Locate every malaria parasite and identify its life-cycle stage.
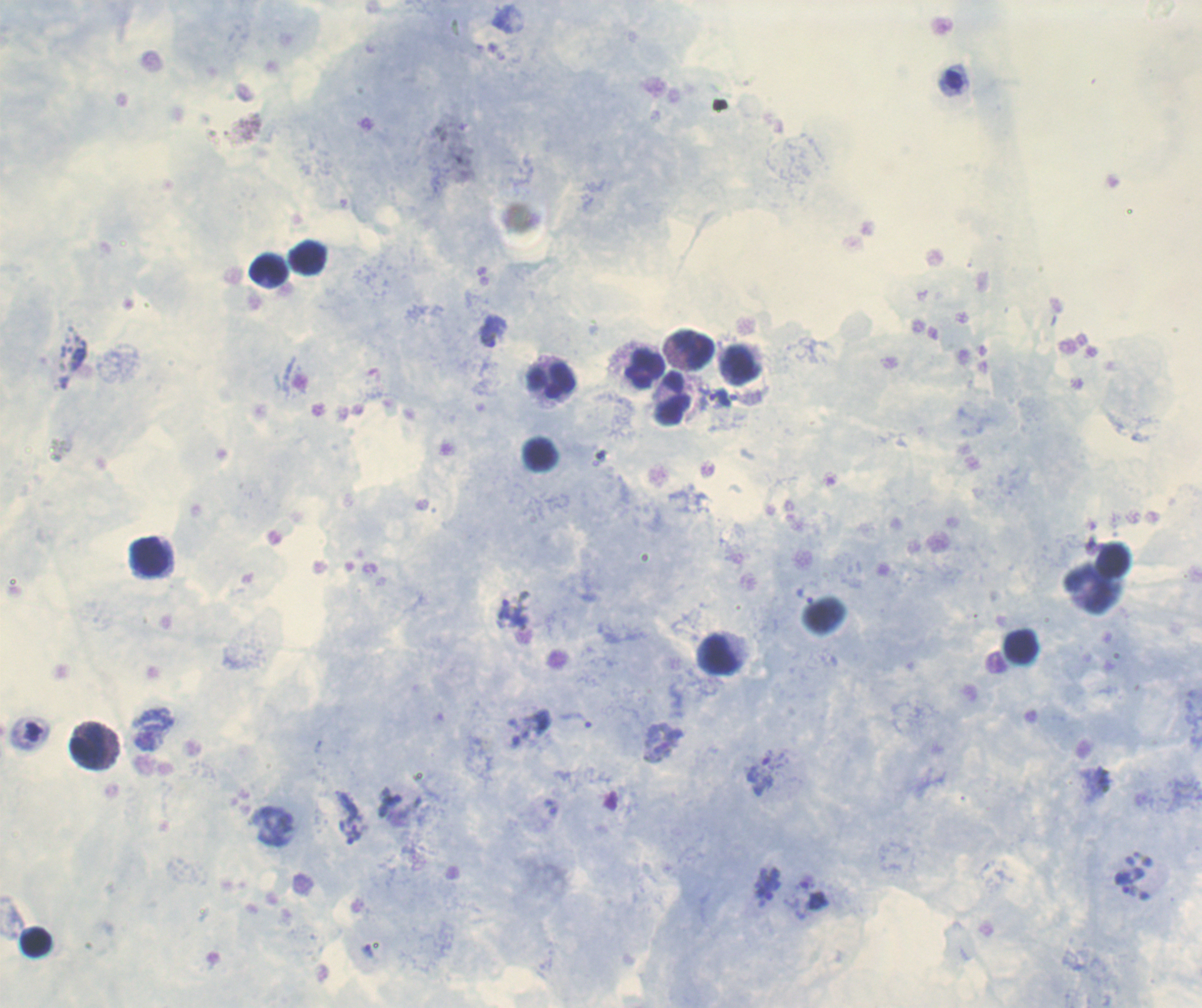

Approximate centers as [x, y] in pixels.
Trophozoites: [488, 340], [718, 397], [509, 612], [577, 720], [661, 743], [390, 801].
No schizont or gametocyte forms observed.

Approximate centers as [x, y] in pixels.
Summary:
  - Leukocyte locations: [308, 257], [268, 267], [694, 346], [740, 365], [646, 367], [550, 378], [673, 399], [539, 453], [150, 556], [1111, 558], [1094, 589], [1021, 647], [718, 653], [95, 747], [36, 943]
  - Stain: Romanowsky
  - Magnification: 100x
  - Background quality: satisfactory
  - Context: previously used in a real diagnosis
  - Image size: 1202×1008 pixels
  - Preparation: thick blood film
  - Coloration quality: good
  - Field of view: single